Assess the morphology of the erythrocytes.
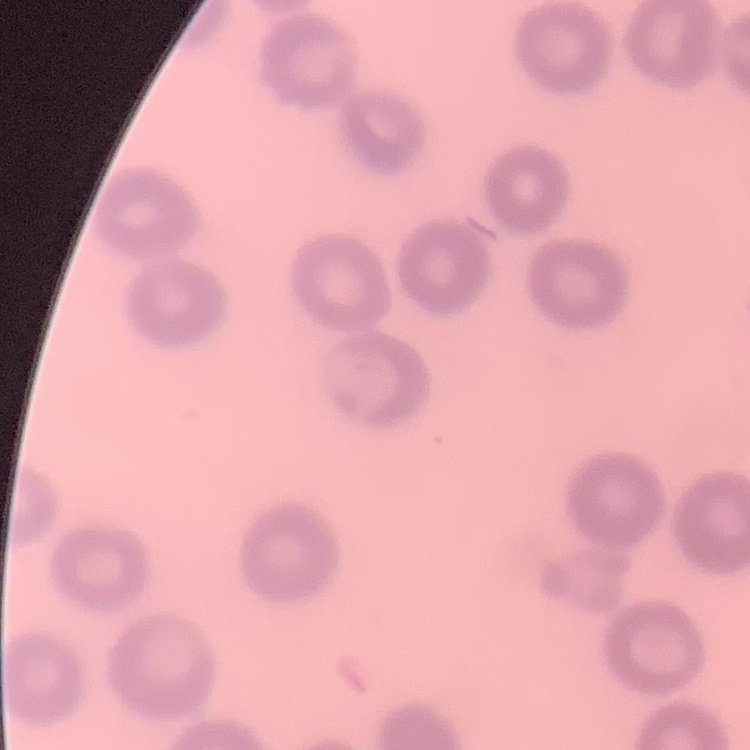

They show no rouleaux formation.

Stained with either Field's or Giemsa. One tile cut from a larger photomicrograph. Thin blood smear.